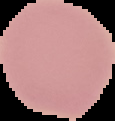 From a thin blood film. Segmented cell region on a black background. Image is 115×121 pixels. Result: no malaria parasites detected.